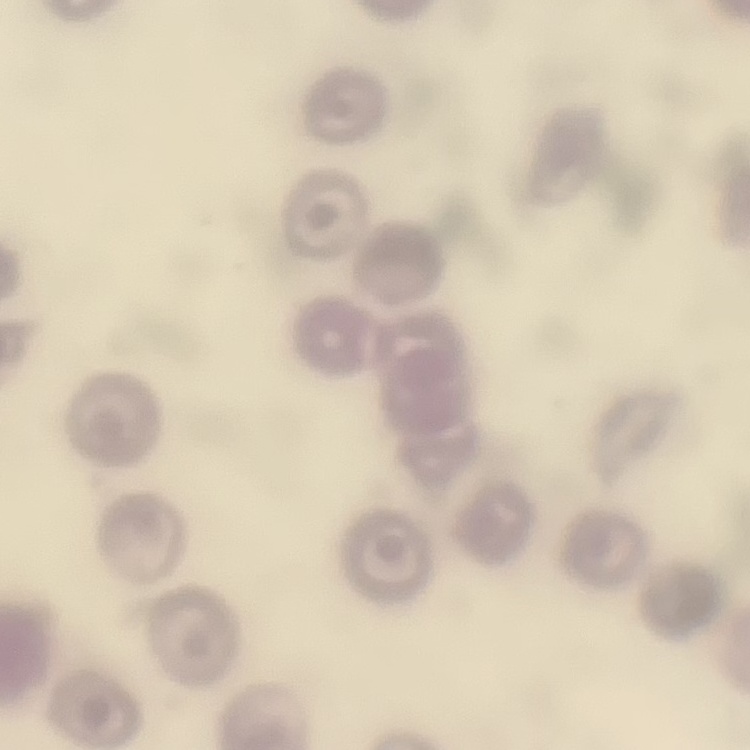
The red blood cells show no rouleaux formation. Thin peripheral smear. Stained with either Field's or Giemsa. Square crop of a larger photomicrograph.